Name the parasite shown.
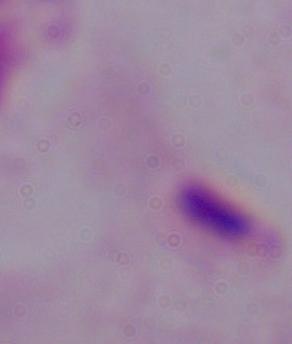
A trichomonad.

Photomicrograph. 1000x magnification.